Point out leukocytes.
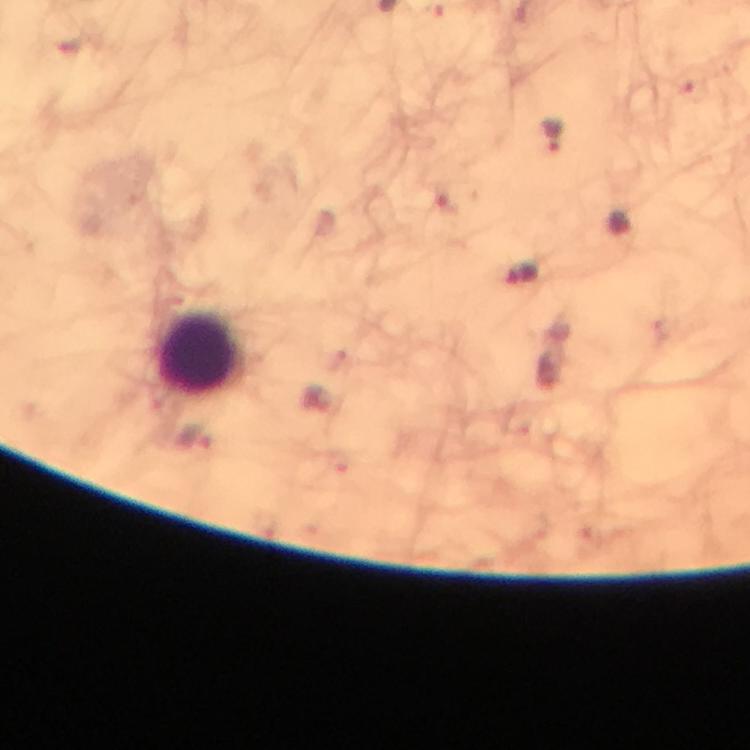

Approximate centers as (x, y) in pixels.
Leukocytes: (202, 353).

Summary:
  - Plasmodium parasite locations: (553, 136), (523, 274), (197, 441)
  - Magnification: 100x
  - Immersion oil: applied
  - Preparation: thick blood film
  - Cropped from: one field of view
  - Stain: Giemsa
  - Image size: 750×750 pixels
  - Context: from a malaria diagnostic workup
  - Capture: smartphone mounted on the microscope